State which parasite is depicted.
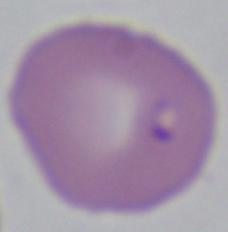

This is Babesia.

Photomicrograph. Captured at 1000x magnification.